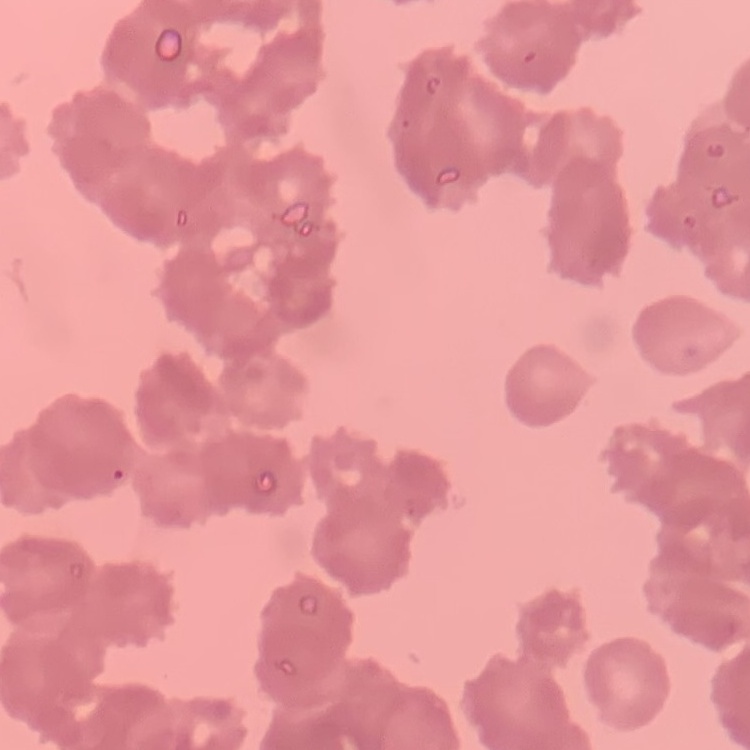
The red blood cells show rouleaux formation. Field's or Giemsa stain. Thin blood film. One tile cut from a larger photomicrograph.